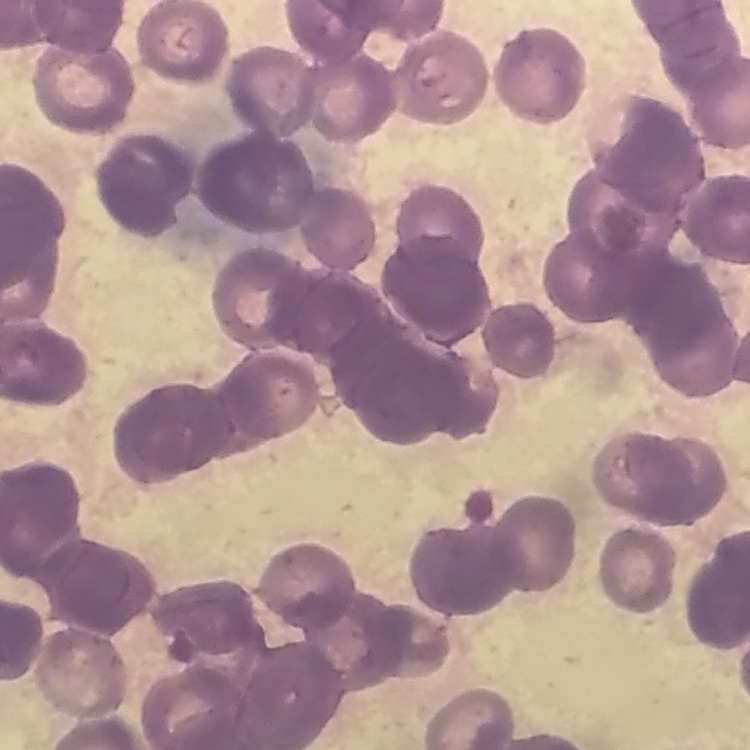
red blood cell morphology = rouleaux formation
preparation = thin blood film
stain = Field's or Giemsa
image type = one tile cut from a larger photomicrograph